Locate and identify every blood parasite.
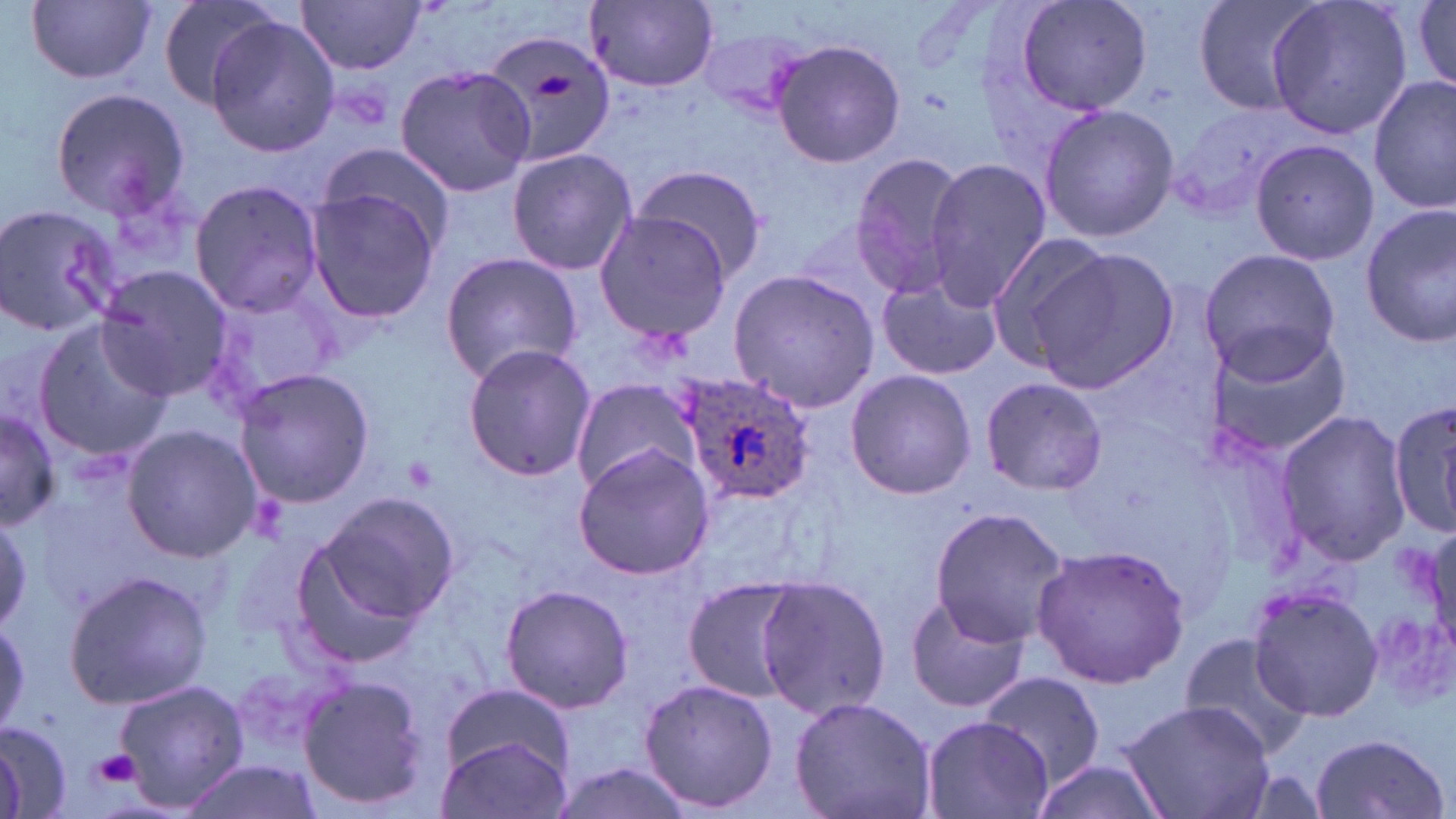

Approximate bounding boxes as (x1, y1, x2, y2) in pixels.
Plasmodium ovale-infected red blood cells: (677, 369, 815, 506).
No Plasmodium falciparum, Plasmodium malariae, Plasmodium vivax, Babesia divergens, or Trypanosoma brucei observed.

slide-level diagnosis = Plasmodium ovale
preparation = thin blood film
magnification = 1000x
stain = May-Grünwald-Giemsa
modality = optical microscopy
image size = 1456×819 pixels
uninfected red blood cell locations = approximate bounding boxes as (x1, y1, x2, y2) in pixels: (26, 0, 156, 84), (155, 0, 283, 110), (1014, 0, 1153, 119), (1190, 0, 1325, 118), (1265, 0, 1413, 138), (297, 1, 428, 73), (585, 1, 720, 90), (1409, 3, 1456, 90), (204, 16, 337, 159), (694, 24, 814, 118), (482, 29, 621, 171), (771, 38, 906, 168), (394, 63, 535, 199), (1370, 74, 1455, 214), (47, 87, 191, 219), (1037, 103, 1178, 243), (1249, 138, 1379, 266), (506, 146, 637, 277), (314, 147, 455, 259), (848, 151, 972, 295), (924, 159, 1053, 308), (628, 162, 768, 281), (188, 178, 326, 318), (305, 185, 443, 323), (0, 202, 124, 340), (1360, 207, 1456, 346), (595, 211, 733, 342), (982, 230, 1119, 366), (1197, 247, 1343, 382), (1026, 248, 1177, 393), (439, 249, 585, 385), (96, 266, 234, 401), (726, 267, 881, 412), (877, 277, 1001, 380), (202, 281, 345, 411), (32, 312, 175, 463), (1202, 324, 1353, 461), (462, 343, 596, 482), (231, 368, 375, 508), (845, 369, 977, 500), (979, 376, 1106, 495), (571, 377, 698, 495), (1386, 399, 1456, 541), (1, 403, 60, 532), (1275, 408, 1412, 568), (122, 425, 263, 561), (573, 442, 718, 580), (300, 489, 459, 649), (927, 507, 1069, 650), (0, 509, 31, 637), (1031, 545, 1191, 688), (64, 567, 211, 709), (755, 574, 890, 722), (682, 577, 804, 702), (498, 583, 633, 715), (1249, 585, 1384, 721), (904, 593, 1028, 714), (1179, 633, 1313, 760), (980, 670, 1105, 787), (296, 674, 431, 812), (112, 677, 250, 813), (638, 677, 778, 814), (441, 682, 577, 783), (790, 696, 937, 819), (1118, 699, 1275, 819), (921, 715, 1055, 819), (0, 719, 71, 819), (1309, 732, 1450, 819), (436, 735, 571, 819), (548, 759, 702, 819), (179, 760, 321, 819), (1029, 761, 1171, 819)
platelet locations = approximate bounding boxes as (x1, y1, x2, y2) in pixels: (532, 71, 575, 99), (93, 749, 141, 787)
field of view = one of a larger specimen